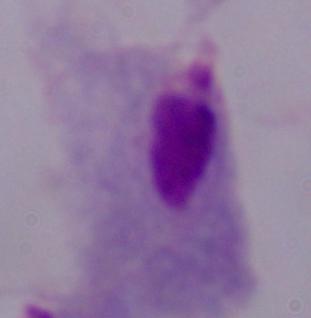
A trichomonad is seen. Captured at 1000x magnification. Micrograph.